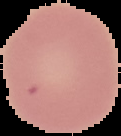

From a thin blood smear. Malaria status: uninfected. Image is 121×136 pixels. The area outside the segmented cell region is set to black.